Report the malaria status of this cell.
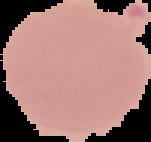
It is uninfected.

Summary:
  - Image type: segmented cell region on a black background
  - Image size: 151×142 pixels
  - Preparation: thin blood smear